Comment on the morphology of the red blood cells.
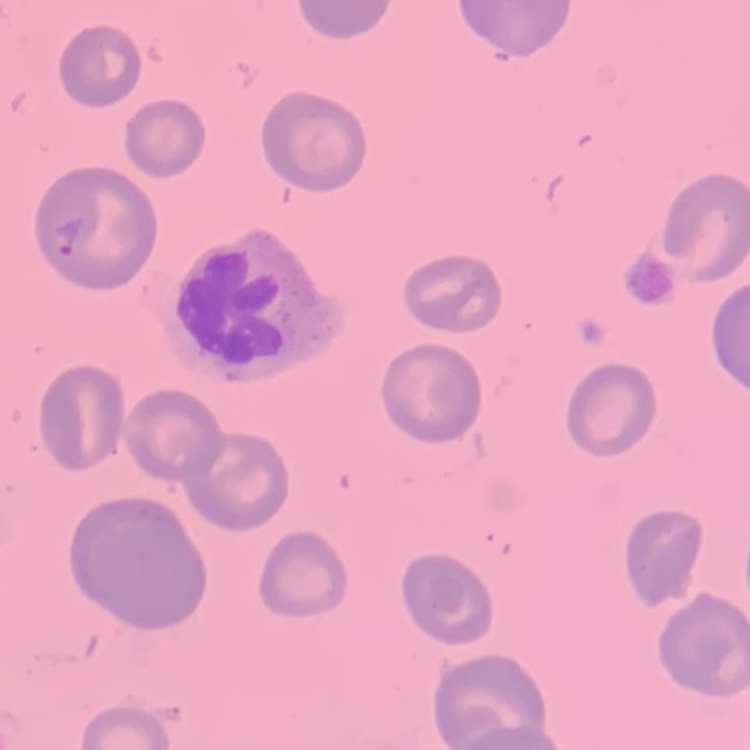
No rouleaux formation.

Summary:
  - Stain: Field's or Giemsa
  - Image type: square crop of a larger photomicrograph
  - Preparation: thin blood film